Assess the morphology of the erythrocytes.
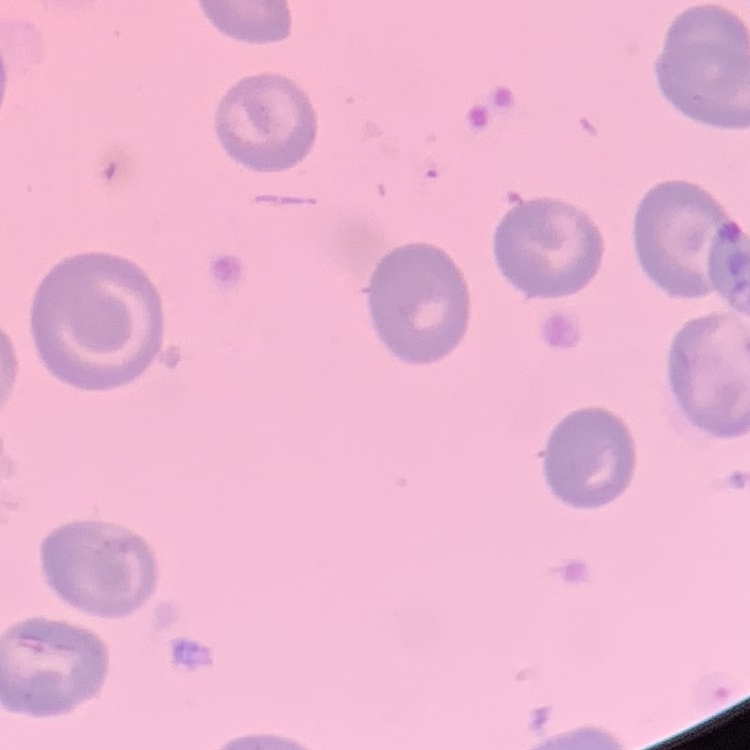

They show no rouleaux formation.

{
  "stain": "Field's or Giemsa",
  "preparation": "thin blood smear",
  "image_type": "one tile cut from a larger photomicrograph"
}